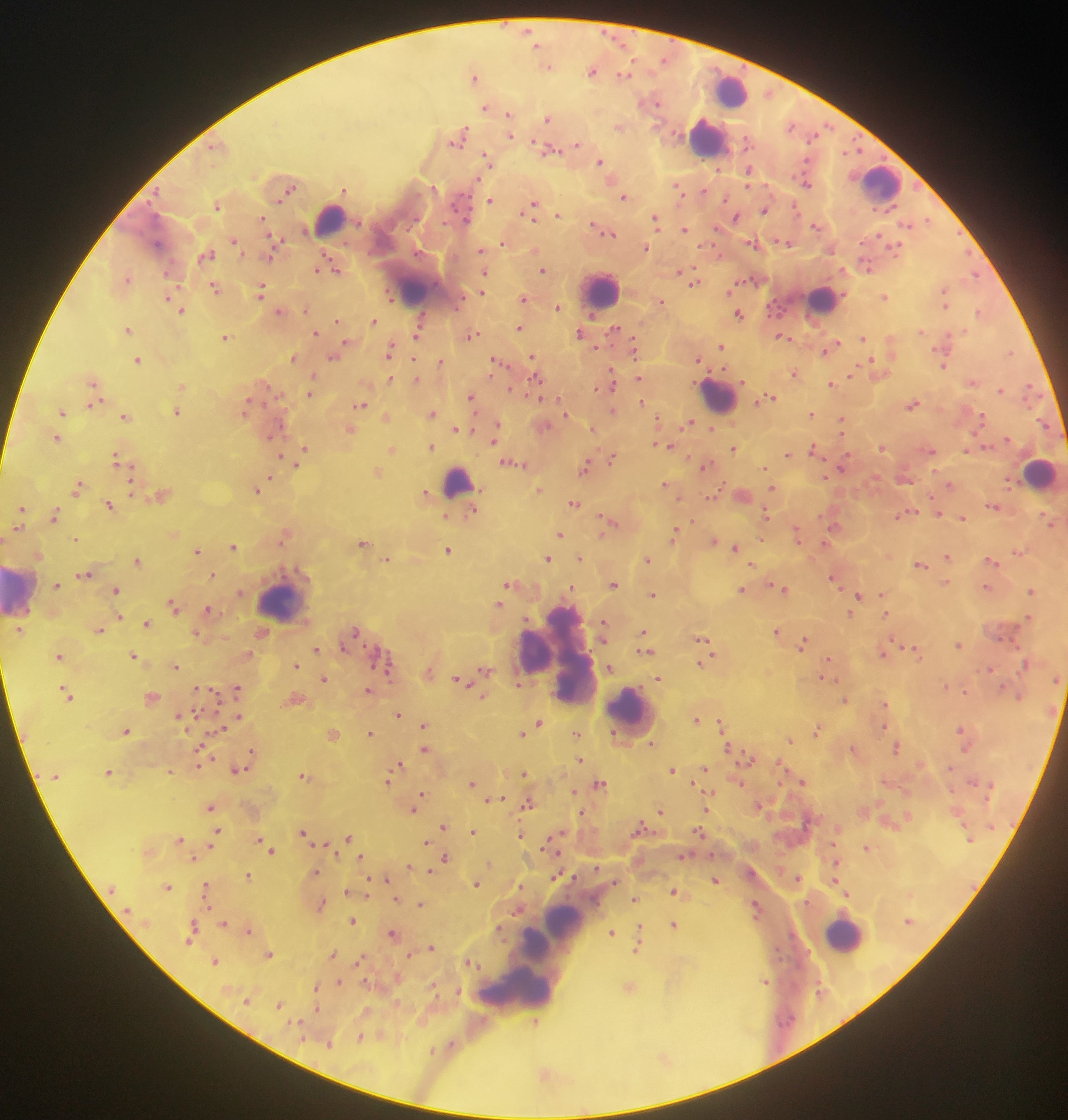

Approximate centers as [x, y] in pixels.
Summary:
  - Leukocyte locations: [731, 90], [708, 138], [881, 182], [329, 219], [415, 286], [601, 289], [821, 300], [718, 395], [1041, 473], [457, 481], [21, 590], [282, 600], [558, 653], [631, 714], [564, 922], [844, 933], [551, 937], [534, 948], [532, 958], [514, 988]
  - Malaria parasite locations: [529, 31], [548, 65], [592, 70], [624, 74], [474, 76], [655, 102], [486, 108], [510, 115], [548, 118], [792, 125], [619, 127], [510, 135], [460, 137], [577, 144], [550, 149], [488, 160], [601, 163], [719, 169], [749, 170], [612, 179], [807, 183], [290, 189], [345, 189], [679, 190], [703, 192], [624, 196], [490, 199], [217, 205], [533, 207], [795, 208], [765, 210], [558, 215], [736, 218], [263, 219], [656, 220], [927, 221], [908, 224], [816, 225], [598, 228], [686, 229], [605, 230], [234, 240], [504, 242], [785, 243], [754, 244], [274, 247], [896, 247], [646, 248], [482, 250], [535, 250], [207, 255], [271, 255], [333, 265], [867, 267], [321, 269], [543, 270], [679, 271], [485, 272], [686, 274], [975, 274], [127, 277], [694, 281], [215, 288], [261, 289], [729, 290], [482, 293], [885, 296], [391, 297], [524, 298], [170, 299], [945, 300], [661, 301], [559, 307], [181, 308], [306, 309], [281, 311], [981, 312], [740, 314], [422, 319], [337, 320], [374, 321], [420, 327], [520, 327], [128, 329], [615, 331], [921, 331], [316, 334], [581, 334], [417, 335], [472, 335], [782, 336], [225, 337], [863, 338], [348, 344], [721, 346], [830, 347], [635, 348], [389, 350], [1010, 352], [334, 356], [294, 357], [533, 357], [415, 358], [698, 359], [139, 360], [442, 361], [498, 361], [874, 364], [943, 364], [794, 374], [852, 374], [314, 376], [611, 376], [390, 378], [536, 378], [640, 378], [417, 379], [972, 381], [95, 383], [832, 383], [182, 386], [598, 388], [1030, 388], [513, 389], [1001, 389], [311, 392], [472, 397], [770, 398], [95, 399], [641, 401], [95, 404], [361, 404], [913, 404], [246, 407], [613, 410], [62, 412], [177, 412], [433, 413], [566, 413], [812, 413], [386, 416], [126, 417], [982, 418], [658, 419], [688, 423], [841, 423], [498, 425], [545, 426], [592, 428], [713, 428], [456, 429], [351, 430], [496, 431], [273, 434], [57, 438], [494, 439], [659, 445], [432, 446], [669, 446], [882, 447], [734, 448], [306, 449], [814, 449], [393, 450], [931, 450], [967, 451], [788, 454], [281, 457], [116, 458], [611, 458], [300, 461], [513, 461], [586, 466], [705, 466], [842, 466], [765, 467], [377, 473], [826, 476], [270, 478], [905, 478], [951, 484], [666, 485], [78, 486], [772, 488], [133, 489], [257, 489], [539, 490], [426, 493], [162, 494], [742, 495], [711, 498], [575, 503], [109, 504], [993, 507], [21, 508], [472, 511], [906, 513], [938, 513], [55, 514], [766, 514], [446, 516], [962, 517], [692, 520], [1049, 521], [609, 523], [834, 525], [19, 528], [675, 532], [797, 533], [285, 534], [560, 535], [76, 538], [761, 539], [714, 540], [364, 541], [234, 546], [735, 547], [198, 550], [448, 550], [1018, 552], [38, 555], [948, 556], [548, 558], [581, 558], [387, 559], [648, 559], [991, 560], [138, 561], [752, 564], [922, 564], [85, 573], [213, 575], [835, 578], [945, 582], [57, 584], [512, 584], [615, 584], [987, 587], [571, 588], [782, 588], [742, 589], [116, 590], [1031, 591], [882, 593], [653, 594], [857, 595], [173, 604], [500, 604], [209, 610], [852, 613], [886, 613], [120, 617], [527, 618], [1028, 618], [147, 621], [604, 623], [99, 629], [355, 631], [777, 631], [644, 632], [262, 633], [197, 634], [702, 639], [804, 642], [958, 644], [345, 647], [317, 649], [705, 649], [645, 650], [915, 651], [883, 653], [134, 654], [249, 654], [60, 655], [828, 661], [702, 663], [175, 665], [297, 665], [387, 666], [610, 667], [990, 668], [486, 669], [429, 671], [824, 677], [325, 678], [659, 678], [460, 680], [519, 684], [946, 686], [198, 688], [238, 688], [369, 690], [965, 691], [67, 693], [1019, 695], [484, 696], [152, 697], [297, 698], [844, 699], [885, 703], [399, 714], [180, 715], [238, 717], [697, 719], [539, 722], [722, 723], [425, 725], [883, 726], [222, 728], [532, 728], [817, 728], [962, 730], [126, 731], [371, 732], [576, 732], [522, 733], [334, 734], [790, 739], [651, 743], [727, 747], [897, 747], [201, 748], [425, 748], [854, 749], [253, 751], [749, 758], [580, 759], [780, 762], [399, 764], [199, 765], [239, 769], [704, 769], [673, 770], [171, 771], [109, 772], [524, 772], [304, 775], [388, 780], [803, 780], [472, 783], [740, 783], [600, 784], [694, 784], [573, 791], [421, 794], [709, 794], [500, 798], [489, 799], [529, 803], [759, 805], [211, 807], [414, 809], [707, 809], [660, 811], [582, 812], [443, 826], [641, 827], [217, 831], [473, 831], [303, 832], [699, 832], [522, 834], [349, 837], [556, 837], [180, 838], [259, 839], [427, 841], [326, 844], [210, 846], [550, 847], [868, 848], [272, 850], [684, 855], [193, 857], [361, 857], [446, 858], [836, 862], [490, 863], [410, 866], [431, 871], [316, 872], [248, 875], [557, 875], [386, 878], [798, 878], [370, 879], [716, 880], [837, 882], [477, 884], [168, 886], [206, 886], [521, 886], [367, 889], [675, 890], [844, 890], [347, 891], [367, 895], [397, 898], [635, 898], [322, 903], [421, 904], [207, 906], [756, 906], [353, 920], [224, 923], [673, 924], [193, 925], [500, 928], [640, 928], [249, 930], [393, 933], [612, 933], [191, 940], [431, 947], [639, 949], [270, 953], [333, 954], [410, 954], [215, 960], [360, 960], [471, 961], [339, 981], [766, 981], [434, 985], [630, 986], [317, 987], [459, 990], [248, 1001], [279, 1004], [317, 1008], [299, 1021], [535, 1021], [360, 1037], [329, 1043], [451, 1045], [433, 1051], [664, 1058], [546, 1074]
  - Preparation: thick blood film
  - Field of view: single
  - Capture: mobile-phone photograph through a microscope
  - Image size: 1068×1120 pixels
  - Country: Ghana